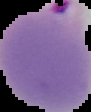 Segmented cell region on a black background. Malaria status: parasitized. From a thin blood film. Image is 91×112 pixels.